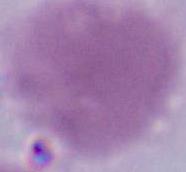
modality: photomicrograph
magnification: 1000x
identification: erythrocyte